Assess for malaria.
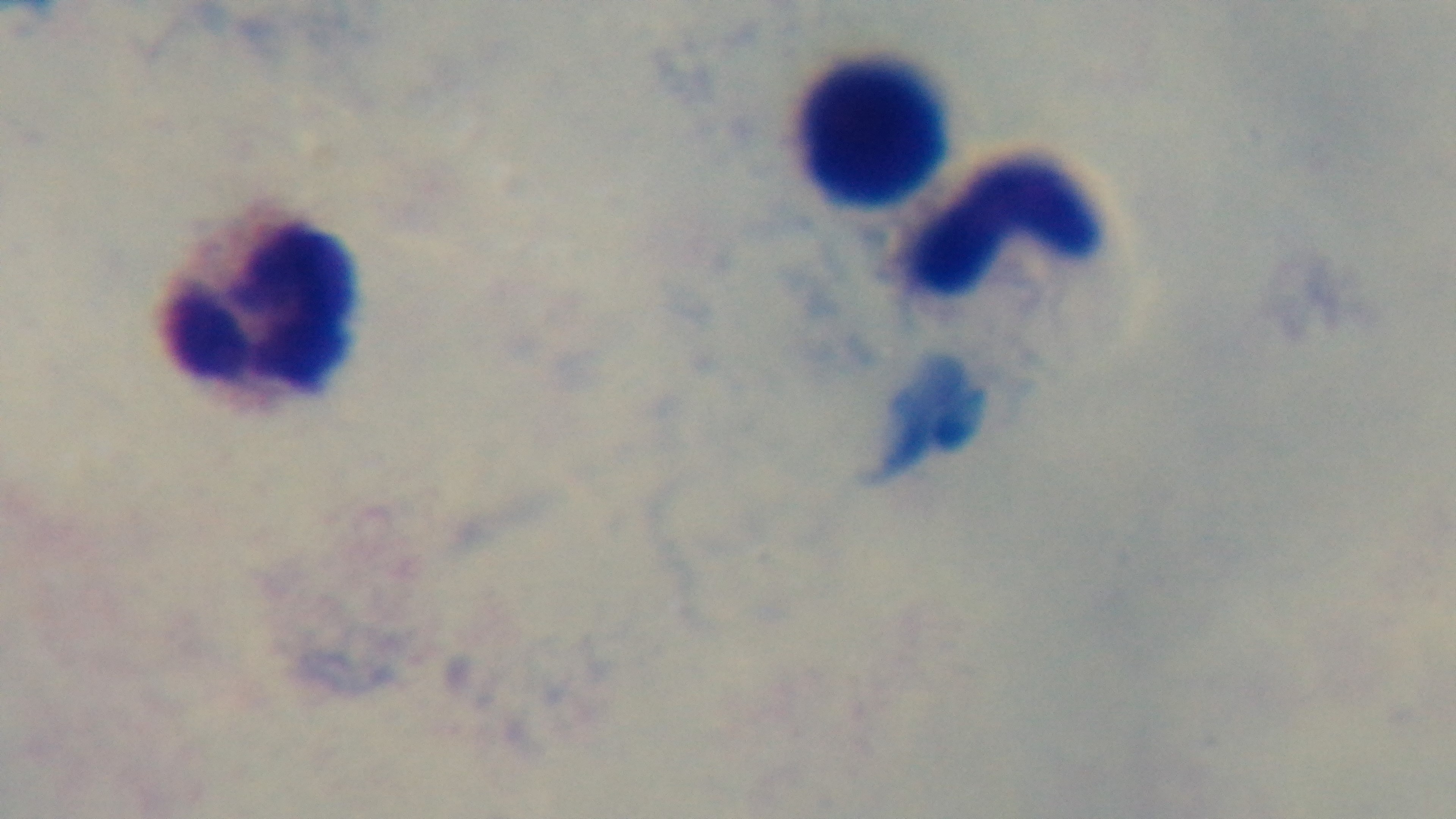

It is uninfected.

Summary:
  - Stain: Giemsa
  - Modality: light microscopy
  - Capture: mounted 4K digital camera
  - Objective: 100x oil immersion
  - Field of view: single
  - Preparation: thick